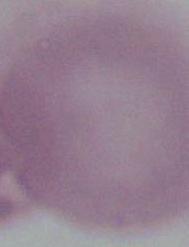

Summary:
  - Magnification: 1000x
  - Identification: erythrocyte
  - Modality: photomicrograph